Assess this cell for malaria.
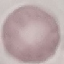

Uninfected.

image type = cell patch, automatically extracted from a larger field of view and resized to 64 × 64 pixels
stain = Giemsa
preparation = thin blood smear
capture = smartphone camera at the microscope eyepiece